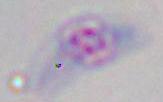

magnification: 1000x
modality: micrograph
identification: Toxoplasma gondii